State the blood parasite species.
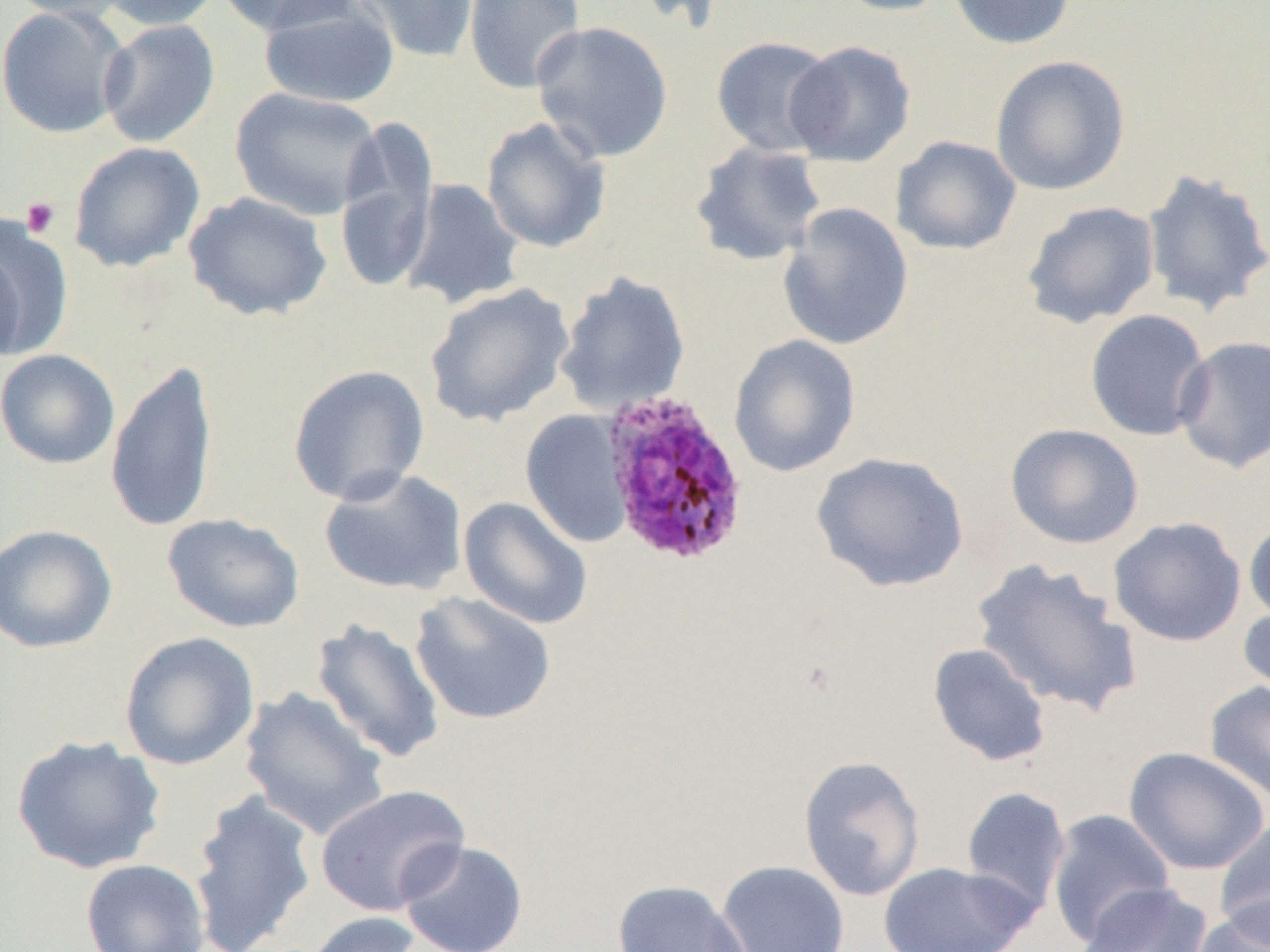

Plasmodium ovale.

{
  "field_of_view": "one of a larger specimen",
  "platelet_locations": "approximate bounding boxes as (x1, y1, x2, y2) in pixels: (20, 196, 60, 239)",
  "uninfected_red_blood_cell_locations": "approximate bounding boxes as (x1, y1, x2, y2) in pixels: (2, 0, 135, 22), (94, 0, 222, 31), (214, 0, 361, 37), (351, 0, 480, 64), (463, 0, 587, 95), (624, 0, 733, 33), (829, 0, 955, 17), (948, 0, 1076, 49), (258, 2, 401, 108), (1, 4, 131, 140), (98, 19, 221, 148), (530, 20, 674, 163), (710, 35, 839, 158), (784, 40, 917, 167), (990, 55, 1131, 196), (229, 87, 383, 221), (480, 116, 611, 254), (335, 117, 440, 294), (891, 135, 1022, 256), (69, 141, 206, 273), (690, 141, 827, 267), (1142, 168, 1270, 318), (399, 178, 524, 310), (183, 191, 334, 321), (1021, 200, 1160, 329), (778, 202, 914, 351), (0, 215, 72, 362), (0, 240, 26, 364), (555, 271, 691, 416), (424, 282, 575, 427), (1084, 310, 1212, 442), (728, 334, 861, 477), (1173, 335, 1270, 473), (0, 349, 120, 469), (105, 359, 219, 535), (287, 364, 430, 505), (519, 409, 634, 548), (1005, 423, 1144, 549), (811, 451, 970, 593), (317, 467, 469, 596), (458, 496, 594, 630), (161, 513, 306, 633), (1243, 515, 1270, 628), (1108, 516, 1247, 647), (0, 524, 118, 653), (970, 559, 1143, 717), (410, 591, 556, 726), (1238, 603, 1270, 709), (311, 617, 446, 764), (119, 631, 260, 771), (927, 642, 1052, 767), (1204, 679, 1270, 804), (238, 687, 390, 840), (11, 734, 166, 874), (1123, 746, 1269, 875), (797, 755, 926, 901), (314, 784, 470, 917), (960, 786, 1071, 914), (187, 790, 318, 952), (1046, 808, 1177, 947), (1214, 818, 1270, 946), (397, 838, 529, 952), (80, 858, 210, 952), (716, 859, 850, 952), (876, 861, 1038, 952), (612, 879, 755, 952), (1075, 883, 1212, 952), (1190, 901, 1270, 952), (302, 911, 428, 952)",
  "preparation": "thin blood film",
  "image_size": "1270×952 pixels",
  "magnification": "1000x",
  "plasmodium_ovale_infected_red_blood_cell_locations": "approximate bounding boxes as (x1, y1, x2, y2) in pixels: (601, 390, 752, 566)",
  "modality": "light microscopy"
}